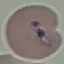

Summary:
  - Result: malaria parasites detected
  - Preparation: thin blood film
  - Image type: automatically extracted cell patch, resized to 64 × 64 pixels
  - Capture: smartphone camera at the microscope eyepiece
  - Stain: Giemsa